Locate and identify every blood parasite.
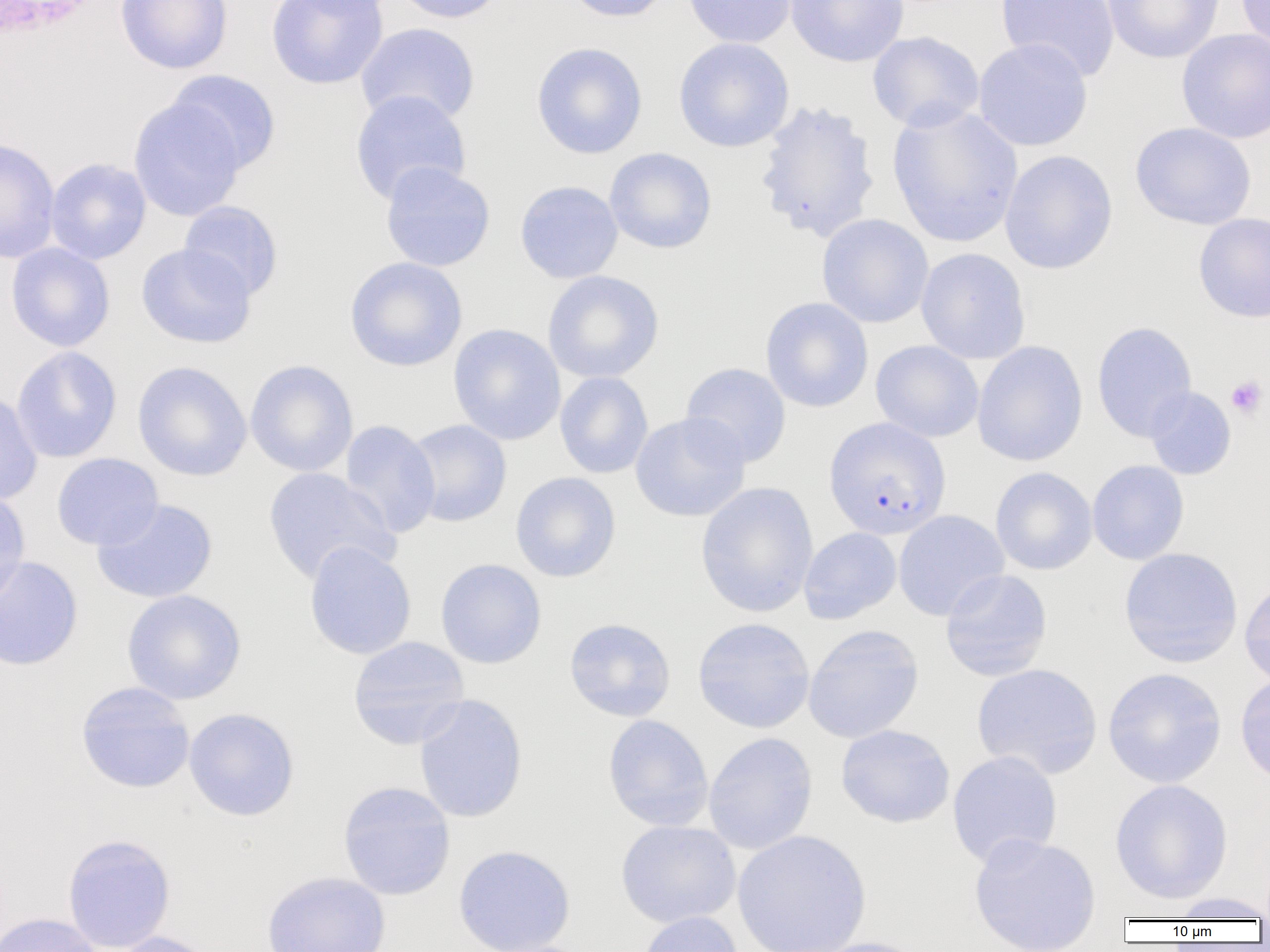

Approximate bounding boxes as [x1, y1, x2, y2] in pixels.
Plasmodium falciparum-infected red blood cells: [824, 417, 951, 540].
No Plasmodium ovale, Plasmodium malariae, Plasmodium vivax, Babesia divergens, or Trypanosoma brucei observed.

Summary:
  - Platelet locations: [1225, 375, 1268, 419]
  - Uninfected red blood cell locations: [115, 0, 233, 74], [266, 0, 388, 90], [390, 0, 508, 24], [562, 0, 675, 23], [682, 0, 797, 48], [785, 0, 909, 67], [996, 0, 1120, 82], [1102, 0, 1225, 63], [1235, 0, 1270, 57], [356, 23, 481, 127], [1176, 28, 1270, 144], [867, 31, 985, 132], [673, 37, 795, 153], [973, 38, 1093, 152], [531, 42, 648, 159], [166, 70, 281, 175], [349, 90, 471, 206], [128, 97, 246, 222], [753, 100, 882, 244], [887, 104, 1023, 248], [1130, 121, 1257, 231], [0, 136, 61, 264], [604, 147, 717, 254], [999, 150, 1119, 275], [45, 158, 151, 265], [380, 161, 496, 272], [514, 180, 623, 283], [178, 200, 284, 301], [1193, 212, 1270, 323], [816, 213, 934, 328], [6, 242, 116, 352], [136, 243, 257, 349], [915, 247, 1031, 364], [344, 256, 468, 372], [542, 270, 664, 383], [760, 297, 874, 413], [1091, 321, 1197, 443], [448, 323, 566, 445], [870, 340, 984, 443], [971, 340, 1088, 467], [11, 346, 122, 463], [245, 359, 359, 477], [132, 361, 252, 481], [680, 362, 792, 468], [555, 372, 653, 479], [1144, 386, 1236, 480], [0, 391, 43, 506], [630, 412, 751, 522], [339, 419, 441, 539], [404, 419, 512, 527], [51, 453, 164, 550], [1087, 460, 1189, 565], [262, 467, 399, 586], [990, 467, 1098, 575], [510, 471, 622, 582], [696, 481, 819, 618], [0, 487, 30, 604], [91, 498, 218, 604], [893, 510, 1009, 621], [798, 527, 902, 624], [304, 541, 417, 660], [1119, 547, 1243, 668], [0, 556, 84, 671], [435, 558, 547, 669], [939, 569, 1053, 681], [1239, 575, 1270, 688], [121, 589, 247, 705], [692, 617, 815, 734], [564, 618, 676, 722], [802, 625, 924, 744], [347, 635, 470, 749], [971, 663, 1103, 779], [1102, 667, 1227, 788], [1235, 672, 1270, 787], [75, 682, 195, 794], [414, 694, 529, 823], [183, 707, 300, 821], [602, 714, 714, 831], [836, 724, 955, 828], [703, 732, 818, 854], [947, 750, 1063, 868], [1109, 779, 1233, 904], [337, 781, 456, 900], [615, 820, 741, 928], [732, 829, 871, 952], [968, 833, 1101, 951], [61, 834, 176, 952], [452, 844, 576, 952], [261, 871, 392, 952], [1167, 892, 1270, 921], [636, 911, 745, 952], [0, 912, 103, 952], [107, 931, 223, 952], [806, 937, 932, 952]
  - White blood cell locations: [0, 1, 113, 46]
  - Slide-level diagnosis: Plasmodium falciparum
  - Preparation: thin blood smear
  - Modality: optical microscopy
  - Image size: 1270×952 pixels
  - Field of view: single
  - Magnification: 1000x